Report the malaria status of this cell.
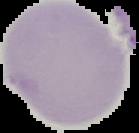
It is uninfected.

image size = 139×133 pixels
image type = segmented cell region with the area outside set to black
preparation = thin blood film